Describe the morphology of the red blood cells.
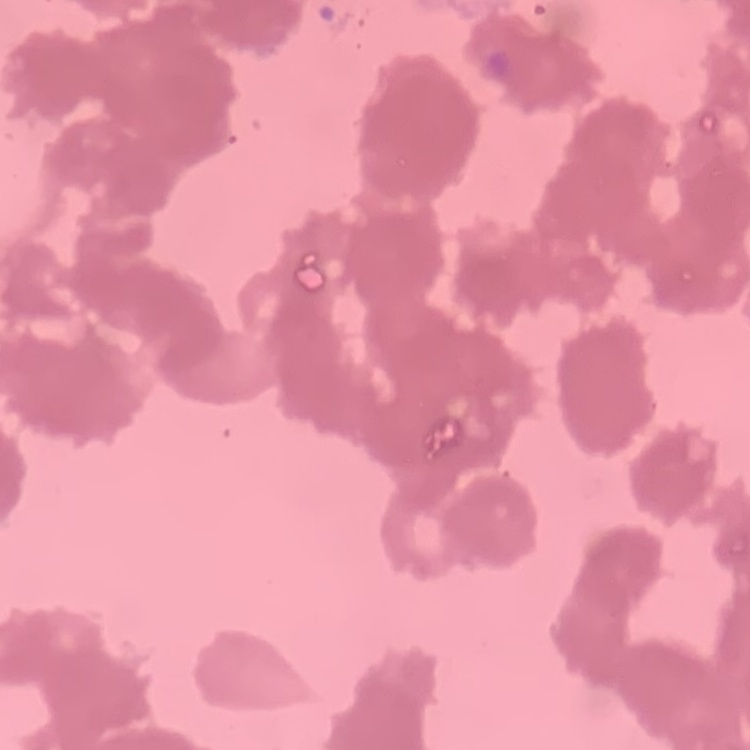

They show rouleaux formation.

Field's or Giemsa stain. Thin blood smear. One tile cut from a larger photomicrograph.